Classify this cell by malaria status.
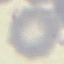

Uninfected.

stain = Giemsa
image type = cell patch, automatically extracted from a larger field of view and resized to 64 × 64 pixels
capture = smartphone through the microscope eyepiece
preparation = thin blood film